Identify the blood parasite species.
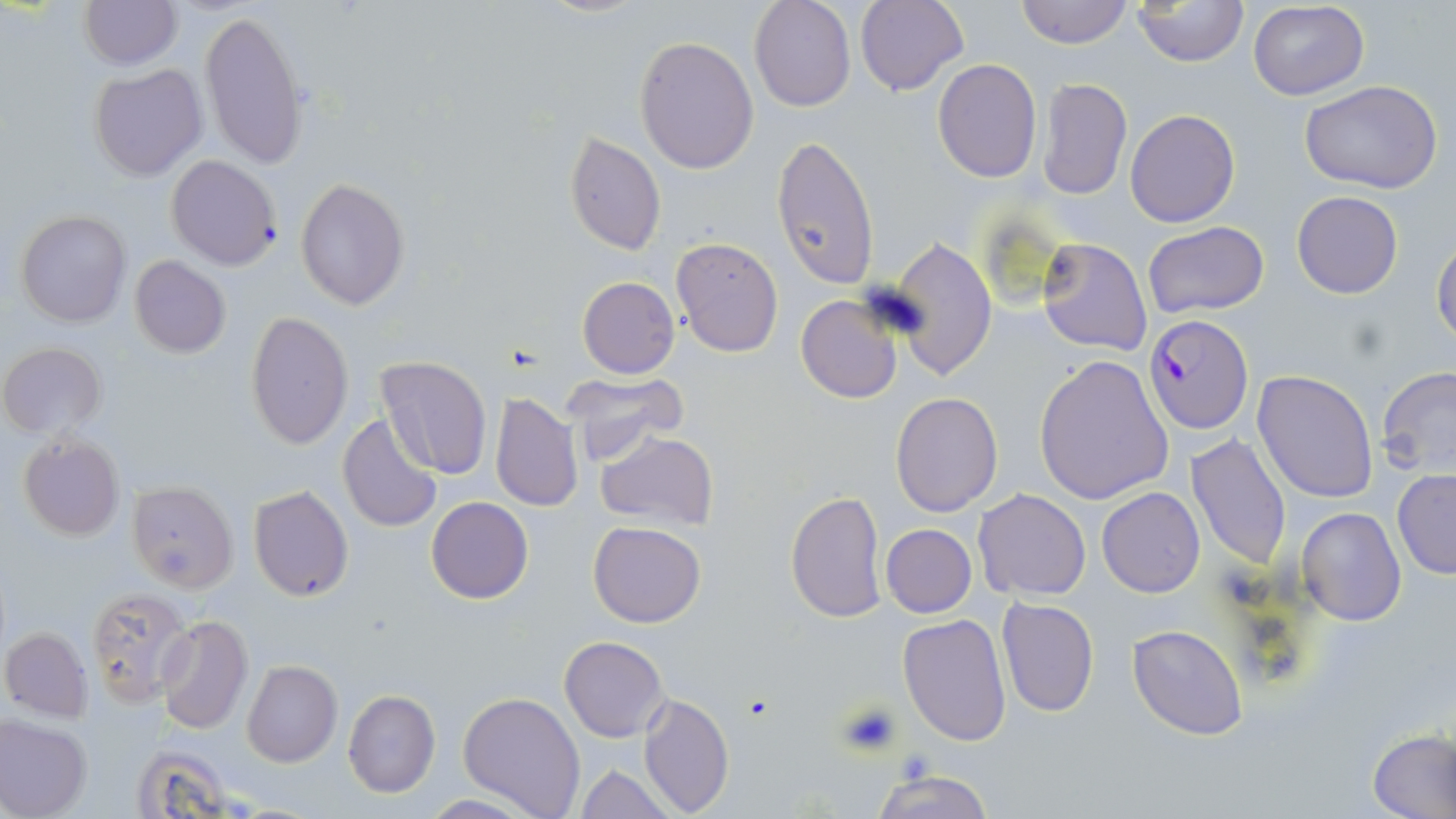
Plasmodium falciparum.

Summary:
  - Coordinate format: approximate bounding boxes as (x1,y1)-(x2,y2) corner pairs in pixels
  - Uninfected red blood cell locations: (79,0)-(181,70), (533,0)-(652,18), (750,0)-(857,111), (856,0)-(968,96), (1013,0)-(1132,48), (1133,1)-(1248,67), (1247,1)-(1370,101), (196,8)-(309,170), (635,35)-(760,175), (932,59)-(1042,183), (89,64)-(207,181), (1037,77)-(1132,201), (1299,79)-(1442,195), (1125,108)-(1240,228), (564,130)-(666,256), (770,135)-(880,290), (166,155)-(282,271), (295,178)-(411,309), (1292,191)-(1403,299), (16,209)-(130,327), (1142,220)-(1271,320), (669,236)-(785,357), (887,237)-(998,381), (1037,237)-(1152,357), (1432,238)-(1456,346), (129,256)-(231,358), (576,275)-(680,378), (797,293)-(902,404), (245,312)-(353,448), (1,342)-(106,438), (374,355)-(492,480), (1034,356)-(1173,503), (1378,366)-(1456,477), (1252,369)-(1379,505), (562,371)-(688,462), (891,390)-(1002,516), (491,392)-(583,513), (336,411)-(445,534), (595,431)-(718,531), (16,434)-(124,542), (1185,434)-(1292,571), (1392,468)-(1456,579), (127,481)-(239,593), (248,484)-(354,602), (1097,486)-(1205,597), (974,489)-(1090,600), (785,490)-(888,623), (426,496)-(534,603), (1297,506)-(1406,627), (588,520)-(707,629), (880,523)-(978,618), (84,588)-(193,706), (995,597)-(1099,717), (898,613)-(1011,746), (155,615)-(255,734), (1127,623)-(1249,740), (2,626)-(92,721), (559,635)-(667,741), (242,661)-(342,767), (341,689)-(440,798), (457,690)-(586,817), (637,691)-(732,818), (0,714)-(92,819), (1366,729)-(1456,819), (129,742)-(250,819), (574,764)-(676,818), (866,770)-(998,819), (417,794)-(539,818)
  - Platelet locations: (834,701)-(903,758)
  - Plasmodium falciparum-infected red blood cell locations: (1144,314)-(1253,435)
  - Preparation: thin blood film
  - Stain: May-Grünwald-Giemsa
  - Field of view: single
  - Image size: 1456×819 pixels
  - Modality: light microscopy
  - Magnification: 1000x